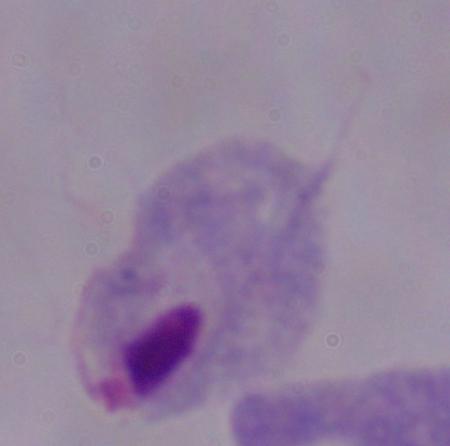
{
  "magnification": "1000x",
  "identification": "trichomonad",
  "modality": "photomicrograph"
}